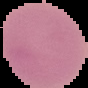
Summary:
  - Preparation: thin blood film
  - Image size: 88×88 pixels
  - Image type: segmented cell region with the area outside set to black
  - Result: negative for Plasmodium parasites